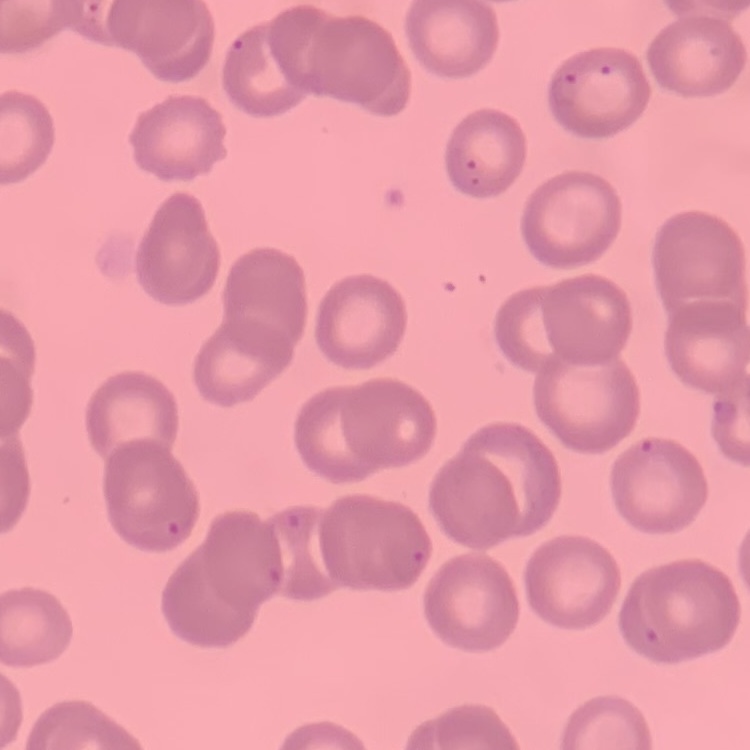

{
  "red_blood_cell_morphology": "no rouleaux formation",
  "stain": "Field's or Giemsa",
  "preparation": "thin blood film",
  "image_type": "square crop of a larger photomicrograph"
}